Assess the morphology of the erythrocytes.
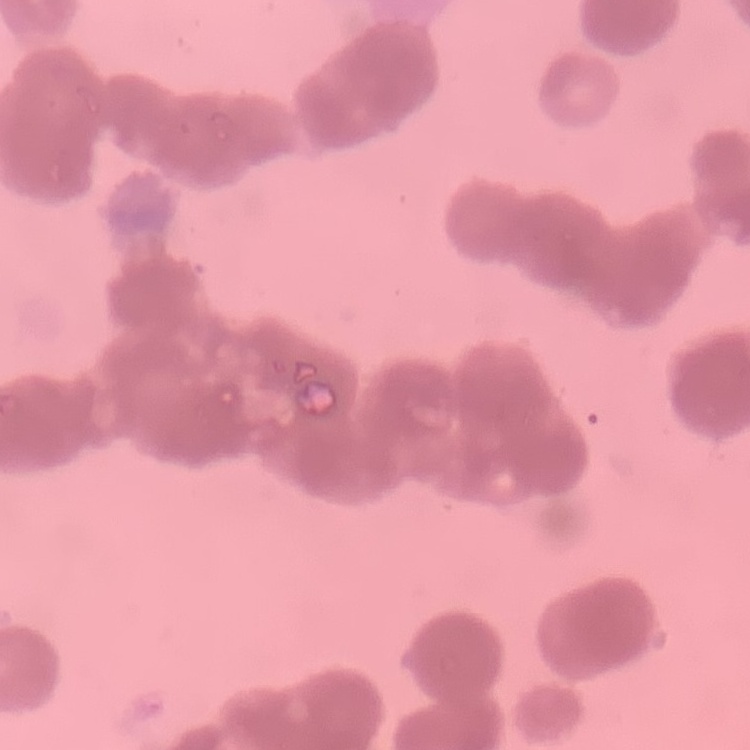
Rouleaux formation.

Summary:
  - Stain: Field's or Giemsa
  - Preparation: thin blood film
  - Image type: one tile cut from a larger photomicrograph